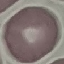

Summary:
  - Result: negative for malaria parasites
  - Preparation: thin blood film
  - Stain: Giemsa
  - Capture: smartphone through the microscope eyepiece
  - Image type: automatically extracted cell patch, resized to 64 × 64 pixels